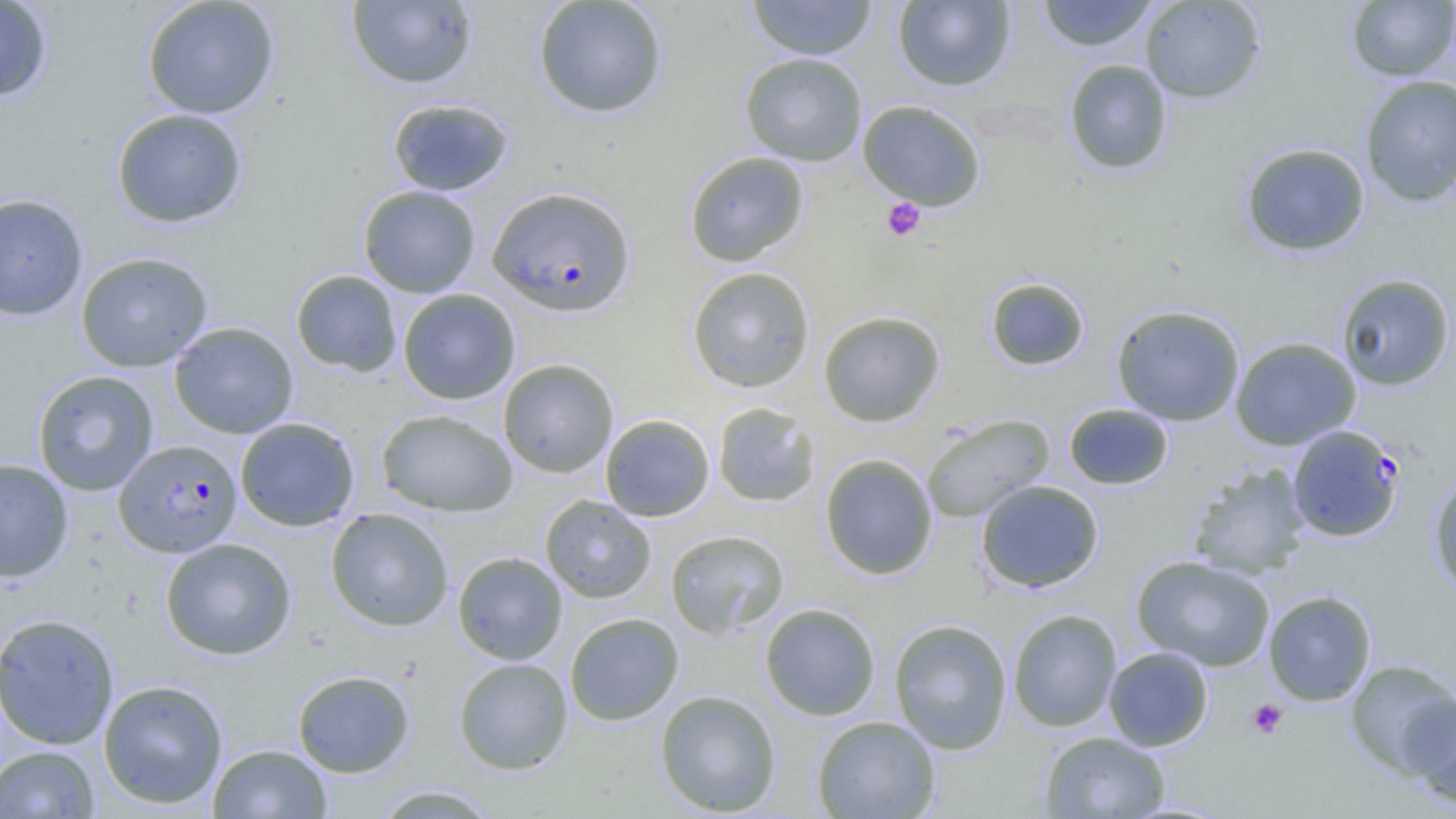
Summary:
  - Coordinate format: approximate bounding boxes as (x1, y1, x2, y2) in pixels
  - Plasmodium falciparum-infected red blood cell locations: (486, 186, 636, 317), (1287, 424, 1405, 542), (113, 439, 242, 557)
  - Platelet locations: (882, 197, 926, 241), (1247, 698, 1289, 740)
  - Uninfected red blood cell locations: (0, 0, 53, 104), (141, 0, 280, 119), (532, 0, 669, 118), (747, 0, 878, 61), (1037, 0, 1160, 51), (1139, 0, 1266, 104), (1346, 0, 1456, 82), (346, 1, 479, 90), (893, 1, 1017, 92), (739, 52, 867, 166), (1063, 59, 1174, 175), (1359, 75, 1456, 207), (386, 98, 515, 196), (857, 100, 987, 210), (110, 108, 248, 228), (1240, 142, 1370, 257), (683, 151, 810, 267), (357, 185, 481, 298), (0, 192, 89, 321), (74, 251, 213, 372), (686, 266, 816, 393), (290, 269, 402, 377), (1336, 273, 1455, 391), (985, 277, 1090, 371), (397, 288, 521, 404), (1110, 304, 1246, 426), (818, 310, 946, 427), (169, 321, 299, 439), (1229, 336, 1361, 450), (498, 358, 618, 478), (32, 370, 159, 496), (712, 402, 820, 508), (1063, 403, 1174, 491), (376, 409, 518, 517), (600, 414, 715, 522), (921, 414, 1055, 523), (235, 417, 360, 532), (820, 453, 937, 580), (0, 457, 74, 582), (1189, 464, 1311, 579), (1428, 472, 1456, 597), (975, 479, 1104, 593), (540, 495, 656, 603), (325, 507, 455, 632), (665, 529, 790, 639), (159, 537, 297, 660), (452, 551, 568, 665), (1131, 555, 1275, 671), (1263, 590, 1377, 706), (760, 603, 881, 721), (1007, 608, 1122, 732), (0, 612, 119, 749), (564, 612, 684, 726), (888, 618, 1013, 754), (1103, 646, 1214, 751), (453, 657, 573, 775), (1344, 659, 1455, 778), (292, 669, 415, 777), (98, 679, 228, 809), (654, 689, 783, 817), (1402, 694, 1456, 809), (811, 715, 941, 819), (1039, 731, 1171, 818), (208, 743, 332, 819), (0, 745, 100, 818), (371, 784, 501, 818)
  - Slide-level diagnosis: Plasmodium falciparum
  - Field of view: one of a larger specimen
  - Image size: 1456×819 pixels
  - Magnification: 1000x
  - Modality: light microscopy
  - Preparation: thin blood smear